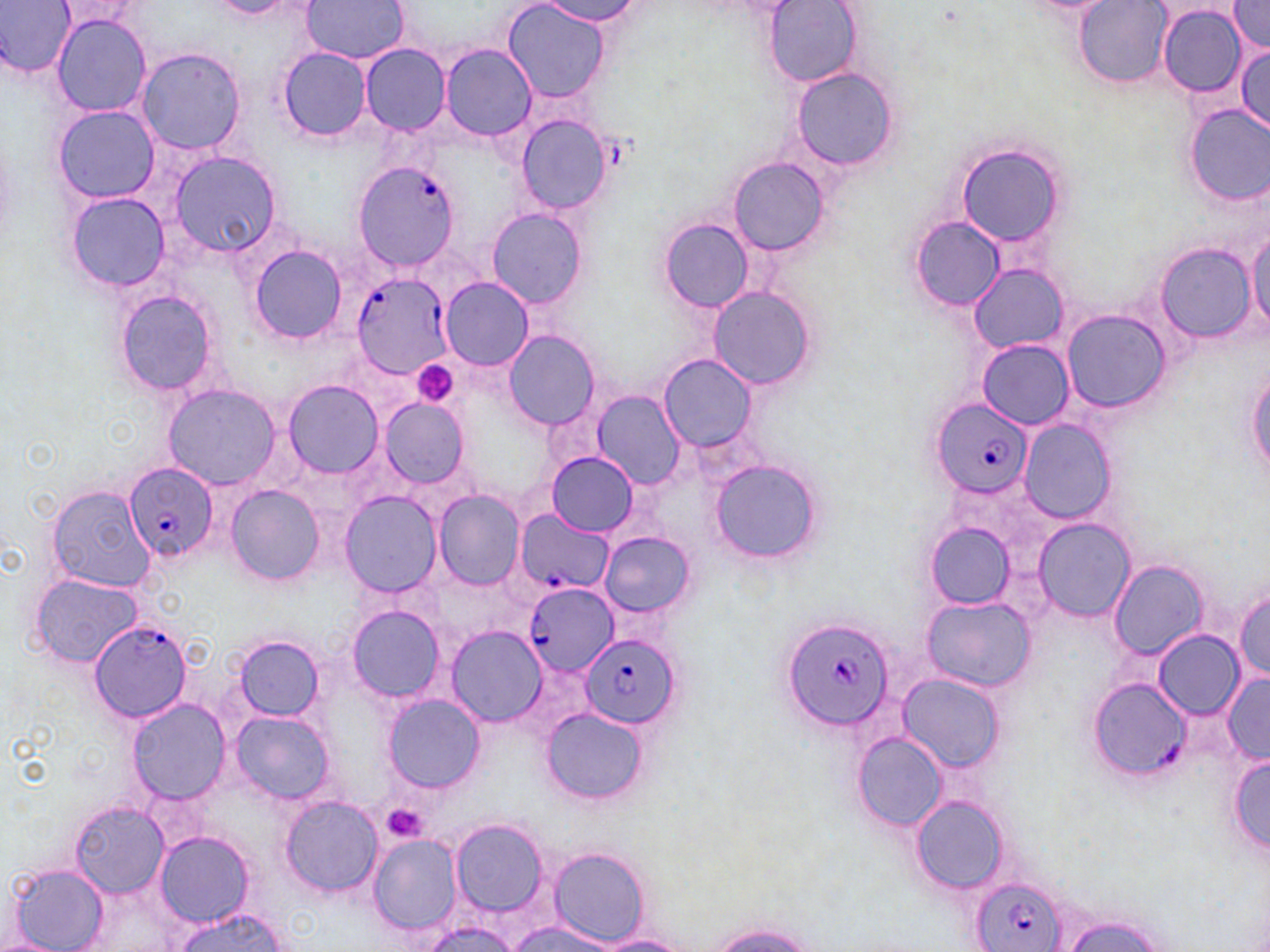
Summary:
  - Coordinate format: approximate bounding boxes as named x1/y1/x2/y2 corners in pixels
  - Uninfected red blood cell locations: (x1=0, y1=0, x2=75, y2=77), (x1=301, y1=0, x2=409, y2=63), (x1=541, y1=0, x2=646, y2=26), (x1=1227, y1=1, x2=1270, y2=53), (x1=208, y1=2, x2=292, y2=18), (x1=502, y1=2, x2=610, y2=102), (x1=765, y1=2, x2=863, y2=86), (x1=1076, y1=2, x2=1169, y2=85), (x1=54, y1=3, x2=148, y2=32), (x1=1157, y1=5, x2=1245, y2=97), (x1=287, y1=7, x2=397, y2=128), (x1=51, y1=14, x2=151, y2=117), (x1=1235, y1=44, x2=1270, y2=133), (x1=359, y1=45, x2=451, y2=135), (x1=440, y1=45, x2=535, y2=140), (x1=134, y1=46, x2=249, y2=155), (x1=277, y1=48, x2=371, y2=141), (x1=791, y1=70, x2=899, y2=170), (x1=1185, y1=104, x2=1270, y2=205), (x1=52, y1=106, x2=160, y2=203), (x1=513, y1=113, x2=615, y2=216), (x1=956, y1=142, x2=1066, y2=249), (x1=166, y1=149, x2=284, y2=258), (x1=727, y1=156, x2=831, y2=258), (x1=65, y1=191, x2=169, y2=291), (x1=485, y1=206, x2=590, y2=310), (x1=909, y1=215, x2=1005, y2=311), (x1=658, y1=217, x2=755, y2=312), (x1=1247, y1=224, x2=1270, y2=334), (x1=1154, y1=244, x2=1257, y2=341), (x1=249, y1=245, x2=348, y2=344), (x1=969, y1=264, x2=1068, y2=353), (x1=440, y1=277, x2=534, y2=370), (x1=707, y1=286, x2=818, y2=391), (x1=113, y1=288, x2=220, y2=396), (x1=1061, y1=307, x2=1169, y2=412), (x1=504, y1=331, x2=600, y2=430), (x1=977, y1=339, x2=1074, y2=430), (x1=659, y1=354, x2=757, y2=449), (x1=1246, y1=364, x2=1270, y2=483), (x1=282, y1=379, x2=383, y2=479), (x1=164, y1=383, x2=281, y2=490), (x1=593, y1=392, x2=687, y2=489), (x1=378, y1=398, x2=469, y2=489), (x1=1020, y1=420, x2=1118, y2=523), (x1=547, y1=452, x2=637, y2=535), (x1=707, y1=458, x2=826, y2=566), (x1=45, y1=485, x2=159, y2=592), (x1=226, y1=485, x2=324, y2=584), (x1=435, y1=491, x2=525, y2=591), (x1=341, y1=492, x2=443, y2=599), (x1=1033, y1=517, x2=1136, y2=622), (x1=925, y1=523, x2=1016, y2=608), (x1=598, y1=530, x2=697, y2=620), (x1=1108, y1=560, x2=1209, y2=659), (x1=28, y1=574, x2=145, y2=670), (x1=1233, y1=586, x2=1270, y2=684), (x1=921, y1=596, x2=1035, y2=692), (x1=343, y1=601, x2=450, y2=706), (x1=446, y1=626, x2=546, y2=727), (x1=1155, y1=632, x2=1244, y2=718), (x1=233, y1=636, x2=324, y2=724), (x1=1220, y1=673, x2=1270, y2=763), (x1=897, y1=676, x2=1004, y2=773), (x1=383, y1=695, x2=484, y2=792), (x1=126, y1=699, x2=231, y2=804), (x1=543, y1=708, x2=646, y2=805), (x1=229, y1=711, x2=335, y2=803), (x1=856, y1=733, x2=947, y2=830), (x1=1229, y1=753, x2=1269, y2=856), (x1=912, y1=795, x2=1009, y2=893), (x1=279, y1=796, x2=383, y2=896), (x1=69, y1=800, x2=169, y2=896), (x1=451, y1=818, x2=550, y2=917), (x1=155, y1=831, x2=254, y2=927), (x1=367, y1=833, x2=462, y2=934), (x1=549, y1=847, x2=648, y2=943), (x1=6, y1=862, x2=110, y2=952), (x1=76, y1=873, x2=198, y2=951), (x1=172, y1=909, x2=291, y2=951), (x1=1059, y1=915, x2=1173, y2=952), (x1=504, y1=919, x2=622, y2=951), (x1=416, y1=920, x2=521, y2=952), (x1=705, y1=921, x2=819, y2=951), (x1=593, y1=934, x2=694, y2=951), (x1=0, y1=939, x2=61, y2=952)
  - Platelet locations: (x1=413, y1=361, x2=459, y2=408), (x1=381, y1=804, x2=429, y2=843)
  - Plasmodium falciparum-infected red blood cell locations: (x1=352, y1=161, x2=462, y2=274), (x1=352, y1=272, x2=451, y2=377), (x1=410, y1=361, x2=461, y2=409), (x1=932, y1=398, x2=1033, y2=499), (x1=123, y1=463, x2=216, y2=561), (x1=515, y1=509, x2=613, y2=596), (x1=523, y1=583, x2=619, y2=678), (x1=780, y1=616, x2=894, y2=732), (x1=88, y1=619, x2=194, y2=724), (x1=580, y1=633, x2=679, y2=727), (x1=1088, y1=678, x2=1190, y2=778), (x1=973, y1=876, x2=1067, y2=952)
  - Slide-level diagnosis: Plasmodium falciparum
  - Image size: 1270×952 pixels
  - Stain: May-Grünwald-Giemsa
  - Magnification: 1000x
  - Preparation: thin blood smear
  - Modality: light microscopy
  - Field of view: single